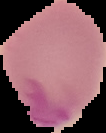

Image is 106×133 pixels. Cell region segmented out of the field of view; the surrounding area is masked to black. Result: no Plasmodium parasites detected. From a thin blood film.